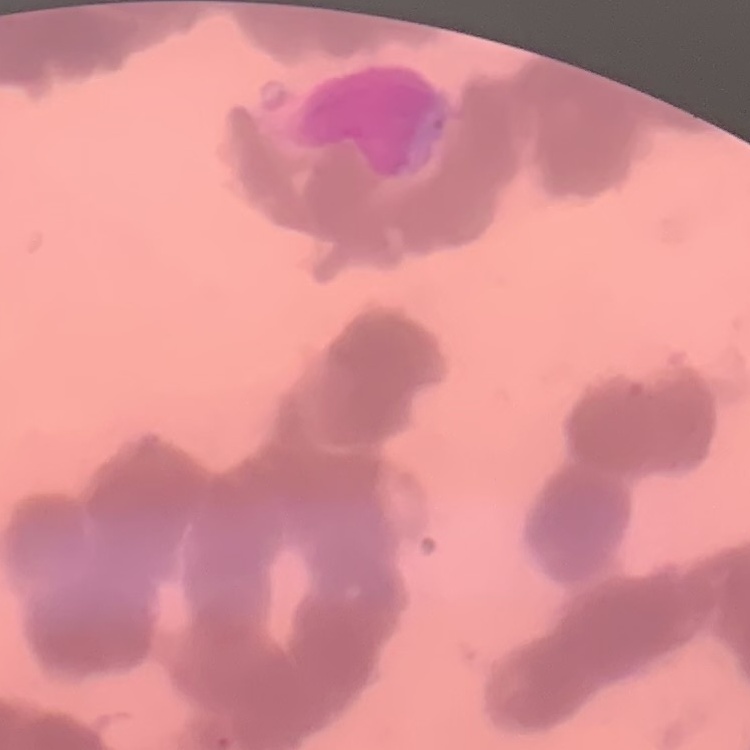

Summary:
  - Erythrocyte morphology: rouleaux formation
  - Image type: one tile cut from a larger photomicrograph
  - Stain: Field's or Giemsa
  - Preparation: thin peripheral smear